Give the position of every leukocyte visible.
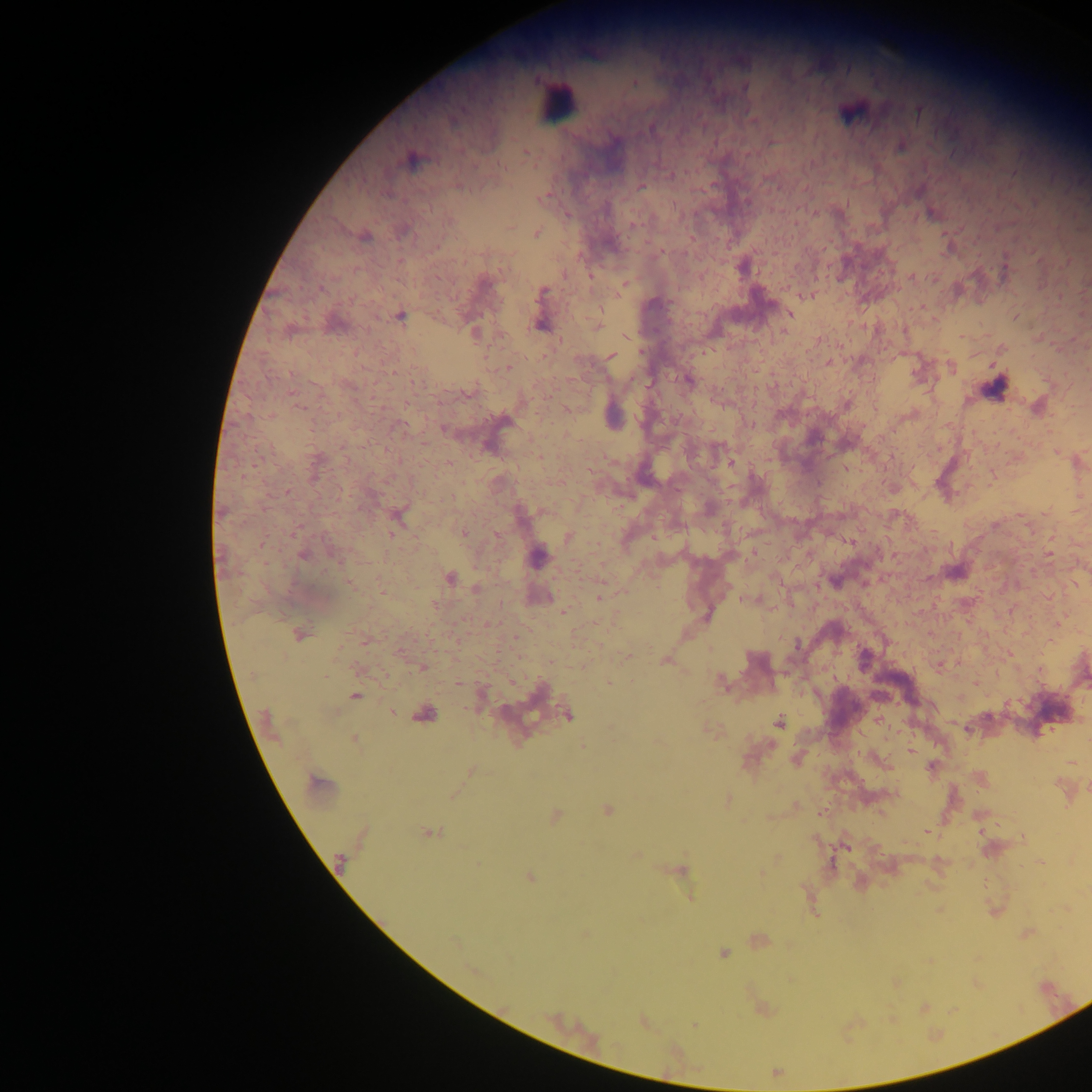
Approximate centers as x y in pixels.
Leukocytes: 556 102.

Malaria parasite locations: 745 87; 918 112; 849 113; 901 147; 526 152; 412 161; 459 186; 642 186; 543 199; 931 212; 449 221; 634 224; 537 233; 365 237; 742 267; 485 283; 624 284; 321 288; 541 293; 806 295; 790 314; 401 317; 539 325; 598 326; 473 332; 611 356; 828 362; 507 367; 688 380; 469 393; 444 429; 732 462; 288 492; 463 533; 569 538; 1049 553; 303 555; 538 557; 954 572; 450 577; 836 582; 350 583; 477 588; 600 598; 749 599; 433 605; 564 612; 706 616; 299 634; 797 646; 864 656; 628 657; 664 661; 422 667; 327 676; 720 682; 458 683; 609 684; 355 697; 391 712; 425 714; 569 716; 779 722; 354 739; 910 751; 931 768; 471 771; 317 782; 727 799; 608 810; 556 816; 429 832; 340 862; 1040 862; 681 871; 530 877; 723 953; 694 1024. Image is 1092×1092 pixels. Single field of view. Sample from Ghana. Thick blood smear. Photographed through a microscope with a mobile-phone camera.